Locate every blood parasite and identify its species.
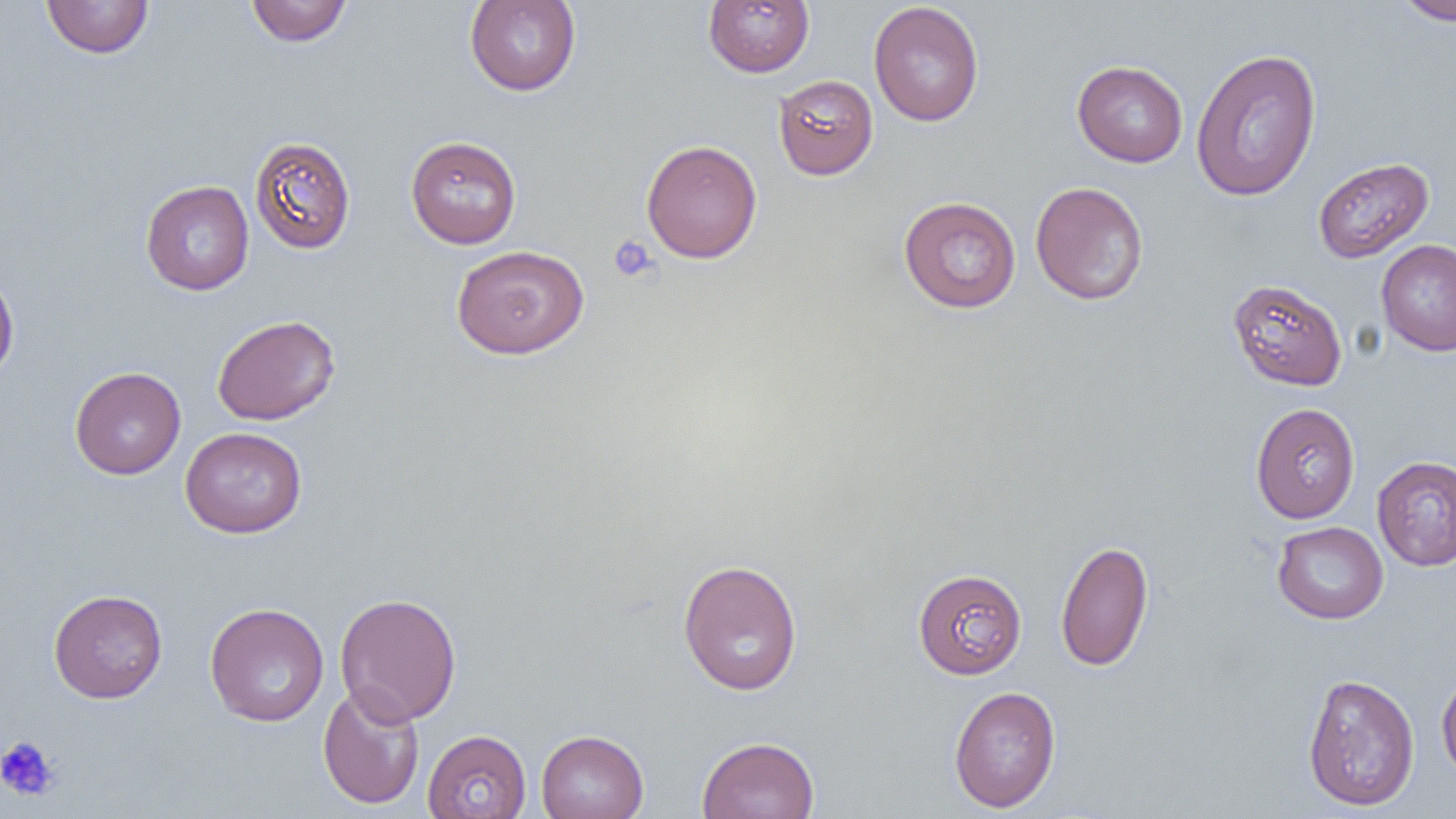

No blood parasites seen.

Approximate bounding boxes as (x1,y1)-(x2,y2) corner pairs in pixels. Uninfected red blood cell locations: (41,0)-(154,58), (464,0)-(581,96), (1392,0)-(1456,26), (245,1)-(353,46), (703,1)-(815,77), (868,2)-(985,127), (1191,47)-(1322,201), (1072,60)-(1188,167), (773,74)-(879,180), (405,135)-(522,248), (249,136)-(356,254), (641,139)-(762,263), (1313,157)-(1434,263), (140,179)-(254,295), (1030,181)-(1149,306), (898,196)-(1022,314), (1376,240)-(1456,356), (451,244)-(589,359), (0,266)-(20,386), (1227,279)-(1347,391), (211,314)-(341,426), (69,366)-(185,480), (1250,402)-(1360,523), (180,427)-(307,538), (1372,456)-(1456,571), (1272,521)-(1388,624), (1055,539)-(1154,672), (677,559)-(803,696), (912,568)-(1027,679), (49,588)-(167,703), (335,592)-(461,726), (204,602)-(329,727), (1436,667)-(1456,784), (1302,672)-(1420,811), (317,683)-(425,810), (949,686)-(1061,812), (422,729)-(531,818), (536,729)-(649,819), (696,735)-(820,819). Platelet locations: (609,235)-(659,282), (0,735)-(60,802). Slide-level diagnosis: negative for blood parasites. Image is 1456×819 pixels. Thin blood smear. Light microscopy. Single field of view. 1000x magnification.